State which parasite is depicted.
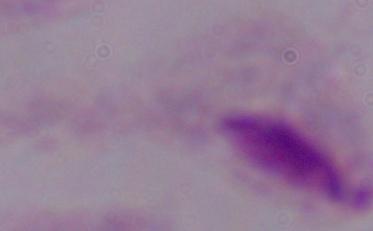

This is a trichomonad.

Micrograph. 1000x magnification.